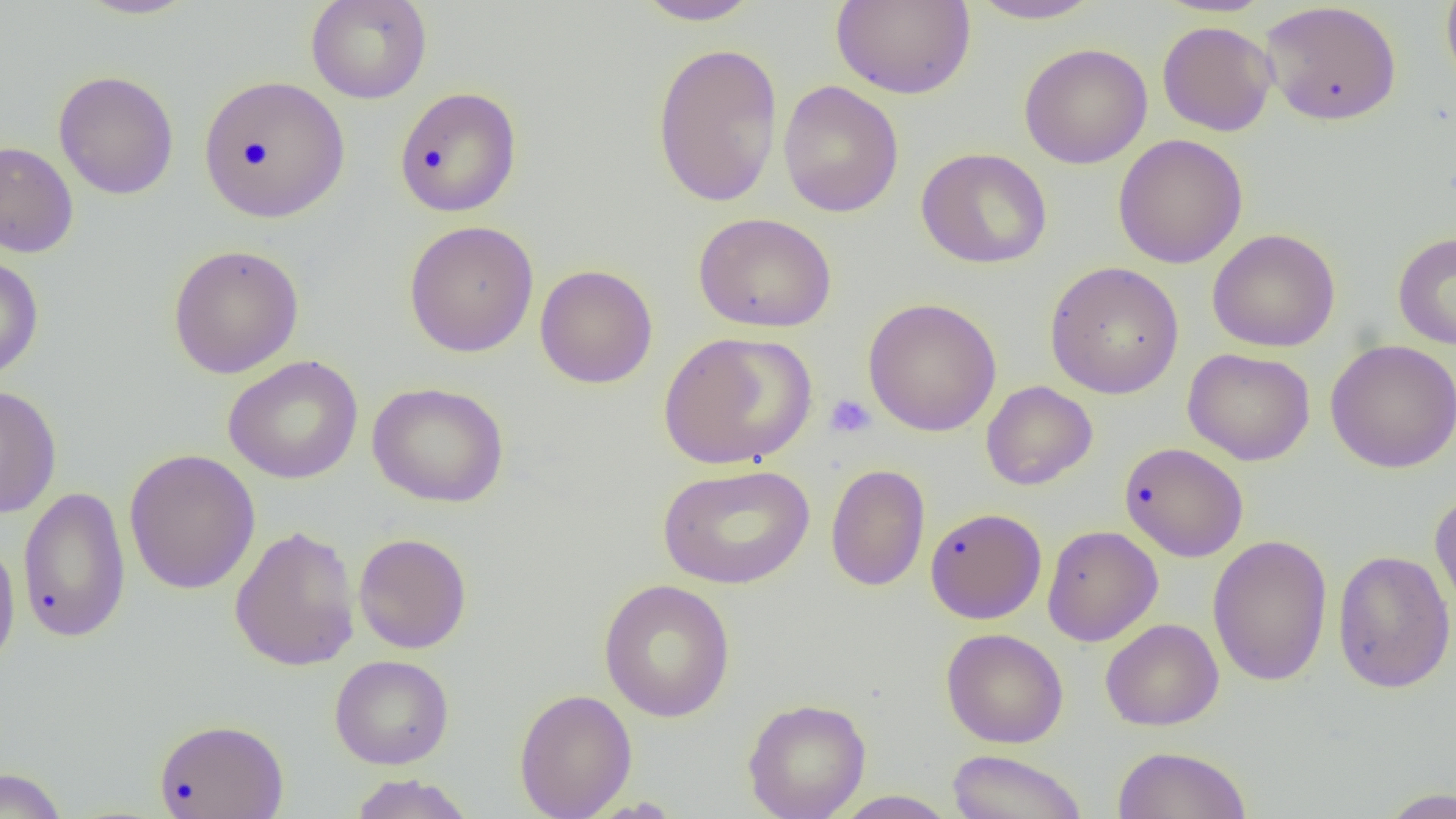
Approximate bounding boxes as [x1, y1, x2, y2] in pixels. Platelet locations: [825, 394, 876, 439]. Uninfected red blood cell locations: [74, 0, 200, 20], [305, 0, 433, 104], [632, 0, 764, 26], [831, 0, 976, 99], [1440, 0, 1456, 93], [967, 1, 1107, 25], [1260, 2, 1402, 126], [1157, 20, 1277, 136], [650, 42, 784, 208], [1019, 43, 1153, 169], [53, 70, 180, 200], [198, 74, 350, 222], [777, 81, 904, 218], [394, 86, 523, 217], [1113, 134, 1248, 269], [0, 140, 79, 258], [916, 147, 1053, 270], [693, 212, 837, 333], [404, 220, 539, 358], [1207, 229, 1340, 352], [1392, 231, 1456, 350], [167, 244, 304, 379], [0, 252, 44, 381], [1044, 261, 1184, 399], [535, 264, 658, 389], [862, 297, 1002, 437], [658, 331, 817, 470], [1325, 339, 1456, 473], [1183, 348, 1315, 466], [223, 355, 363, 484], [980, 380, 1098, 490], [367, 382, 510, 508], [0, 384, 62, 519], [1119, 441, 1249, 562], [123, 448, 261, 595], [657, 463, 815, 589], [825, 464, 931, 591], [16, 486, 132, 643], [1429, 491, 1456, 619], [925, 507, 1047, 624], [1042, 524, 1163, 647], [229, 525, 360, 672], [0, 532, 21, 677], [353, 532, 472, 654], [1207, 533, 1333, 687], [1332, 549, 1455, 693], [598, 578, 736, 723], [1100, 618, 1224, 731], [941, 628, 1068, 748], [330, 654, 454, 769], [514, 688, 637, 819], [742, 698, 871, 819], [154, 717, 289, 819], [1112, 745, 1252, 818], [946, 749, 1089, 819], [0, 767, 68, 819], [348, 773, 476, 819], [1377, 787, 1456, 817], [830, 790, 959, 818]. Slide-level diagnosis: negative for blood parasites. Thin blood smear. One field of a larger specimen. Optical microscopy. Image is 1456×819 pixels. Captured at 1000x magnification.